Assess this cell for malaria.
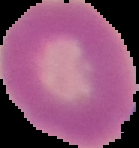
It is uninfected.

{
  "image_type": "cell region segmented out of the field of view; surrounding area masked to black",
  "preparation": "thin blood smear",
  "image_size": "139×148 pixels"
}